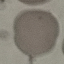

malaria status = uninfected
capture = smartphone through the microscope eyepiece
preparation = thin blood film
stain = Giemsa
image type = automatically extracted cell patch, resized to 64 × 64 pixels